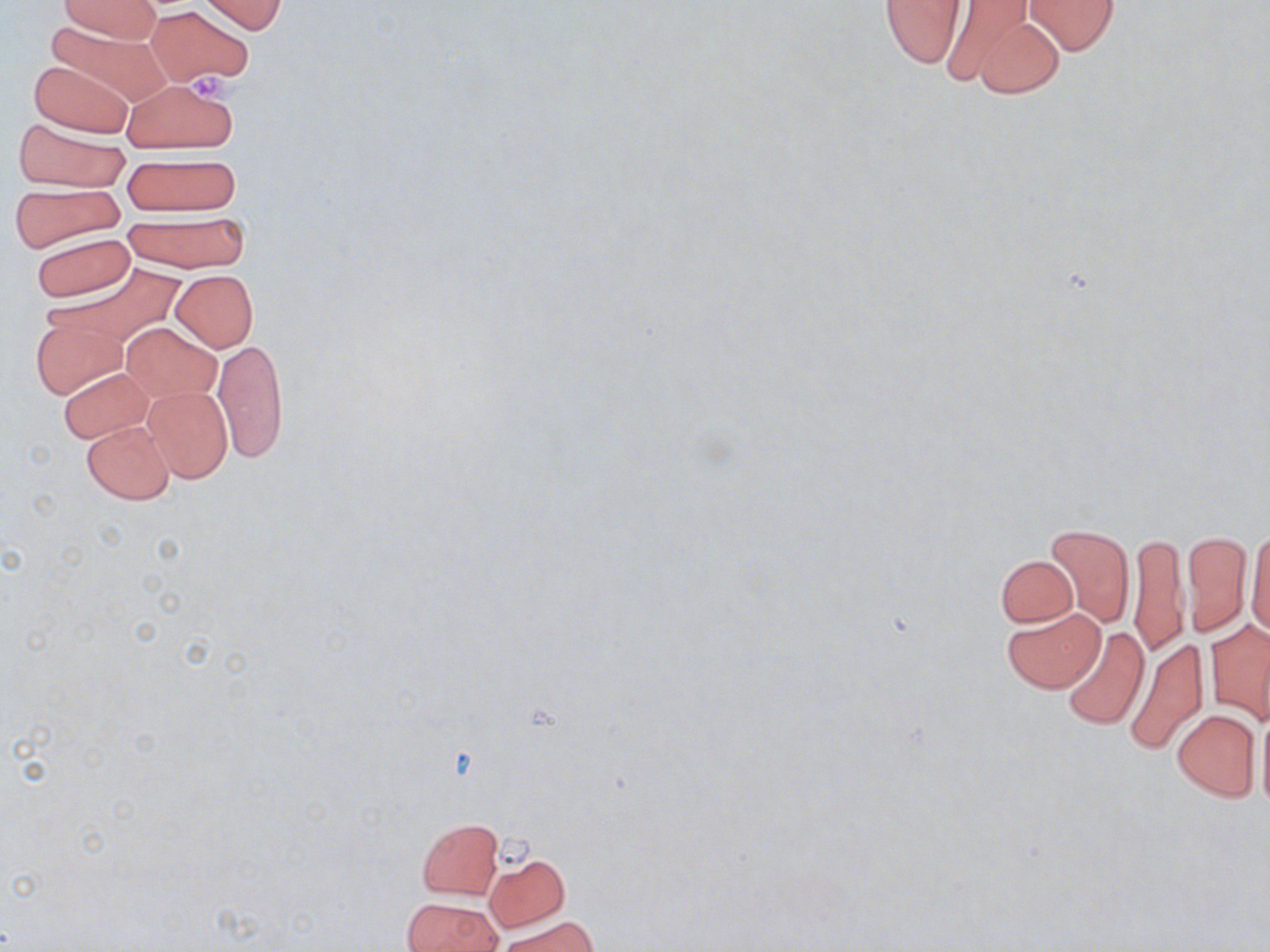

slide-level diagnosis = no evidence of blood parasites
uninfected red blood cell locations = approximate bounding boxes as (x1,y1)-(x2,y2) corner pairs in pixels: (59,0)-(163,42), (200,0)-(286,35), (878,0)-(968,68), (1024,0)-(1121,55), (928,2)-(1039,85), (146,5)-(253,88), (966,14)-(1067,98), (41,21)-(169,107), (27,59)-(133,137), (123,77)-(242,154), (12,117)-(128,192), (121,152)-(240,216), (8,181)-(124,251), (120,213)-(249,273), (31,232)-(136,302), (53,262)-(187,345), (171,270)-(258,351), (31,313)-(126,400), (124,322)-(220,404), (214,337)-(288,463), (58,366)-(154,443), (142,385)-(234,482), (82,420)-(174,504), (1044,521)-(1134,627), (1246,522)-(1270,639), (1182,530)-(1252,635), (1128,532)-(1188,657), (995,555)-(1077,627), (1002,606)-(1106,692), (1206,619)-(1270,724), (1060,626)-(1149,730), (1124,634)-(1210,755), (1256,703)-(1270,813), (1171,709)-(1261,801), (417,818)-(502,898), (484,852)-(570,932), (402,898)-(499,951), (500,916)-(597,952)
modality = light microscopy
preparation = thin blood film
image size = 1270×952 pixels
platelet locations = approximate bounding boxes as (x1,y1)-(x2,y2) corner pairs in pixels: (193,73)-(243,105)
stain = May-Grünwald-Giemsa
field of view = one of a larger specimen
magnification = 1000x